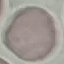

{
  "malaria_status": "uninfected",
  "capture": "smartphone through the microscope eyepiece",
  "preparation": "thin smear",
  "stain": "Giemsa",
  "image_type": "automatically extracted cell patch, resized to 64 × 64 pixels"
}